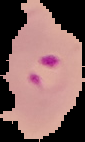
From a thin blood smear. The area outside the segmented cell region is set to black. Image is 85×142 pixels. Malaria status: parasitized.